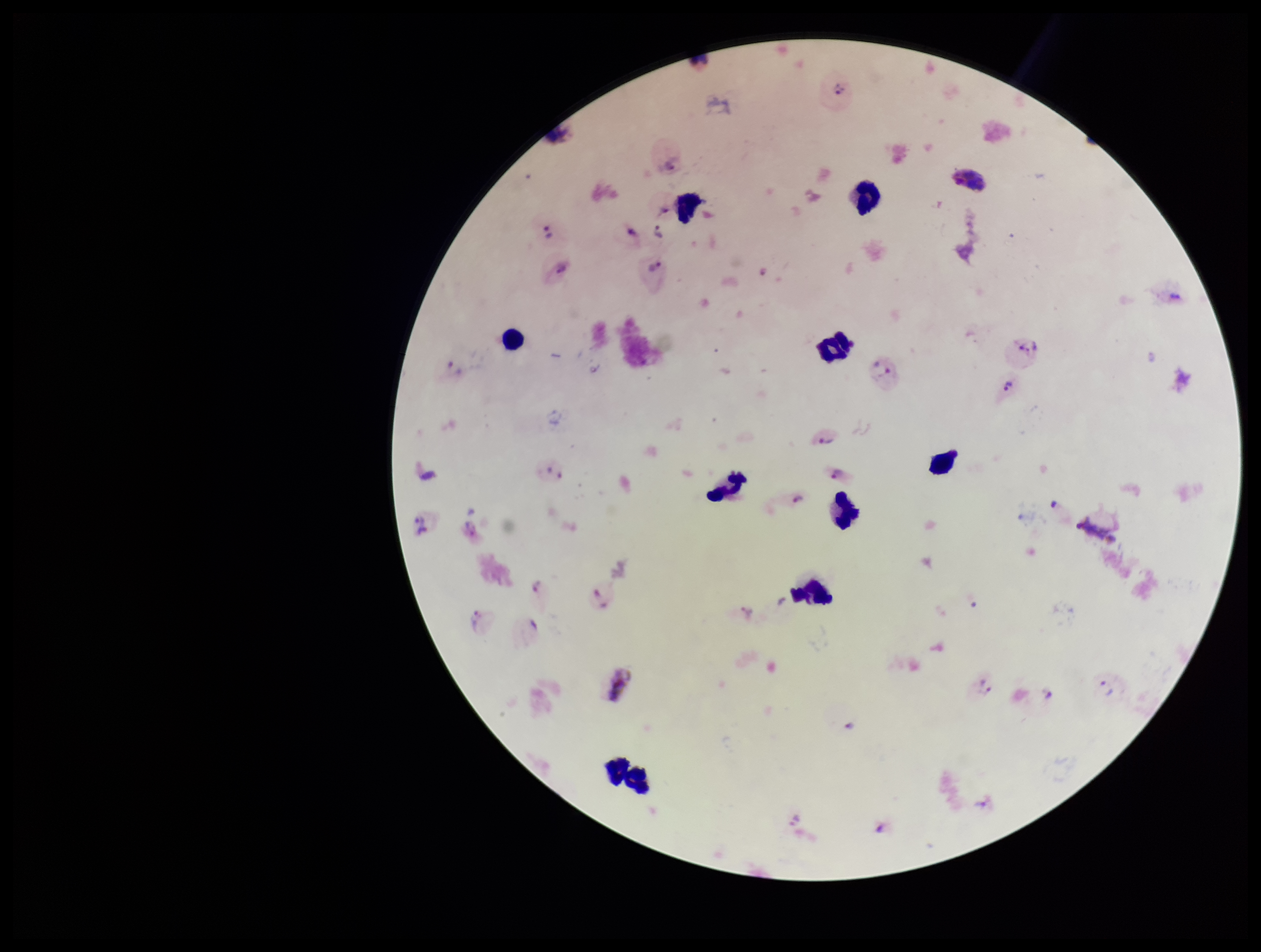
stain = Giemsa
capture = smartphone photograph through the microscope eyepiece
field of view = single
image size = 1261×952 pixels
leukocyte count = 11
patient malaria status = positive
species reported for this patient = Plasmodium vivax
parasite count = 27
Plasmodium parasites = seen
preparation = thick